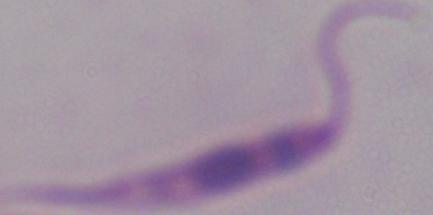 A Leishmania parasite is shown. Micrograph. Captured at 1000x magnification.